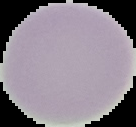

Summary:
  - Preparation: thin blood smear
  - Image size: 136×127 pixels
  - Result: no malaria parasites seen
  - Image type: segmented cell region on a black background